Evaluate for parasitized red blood cells.
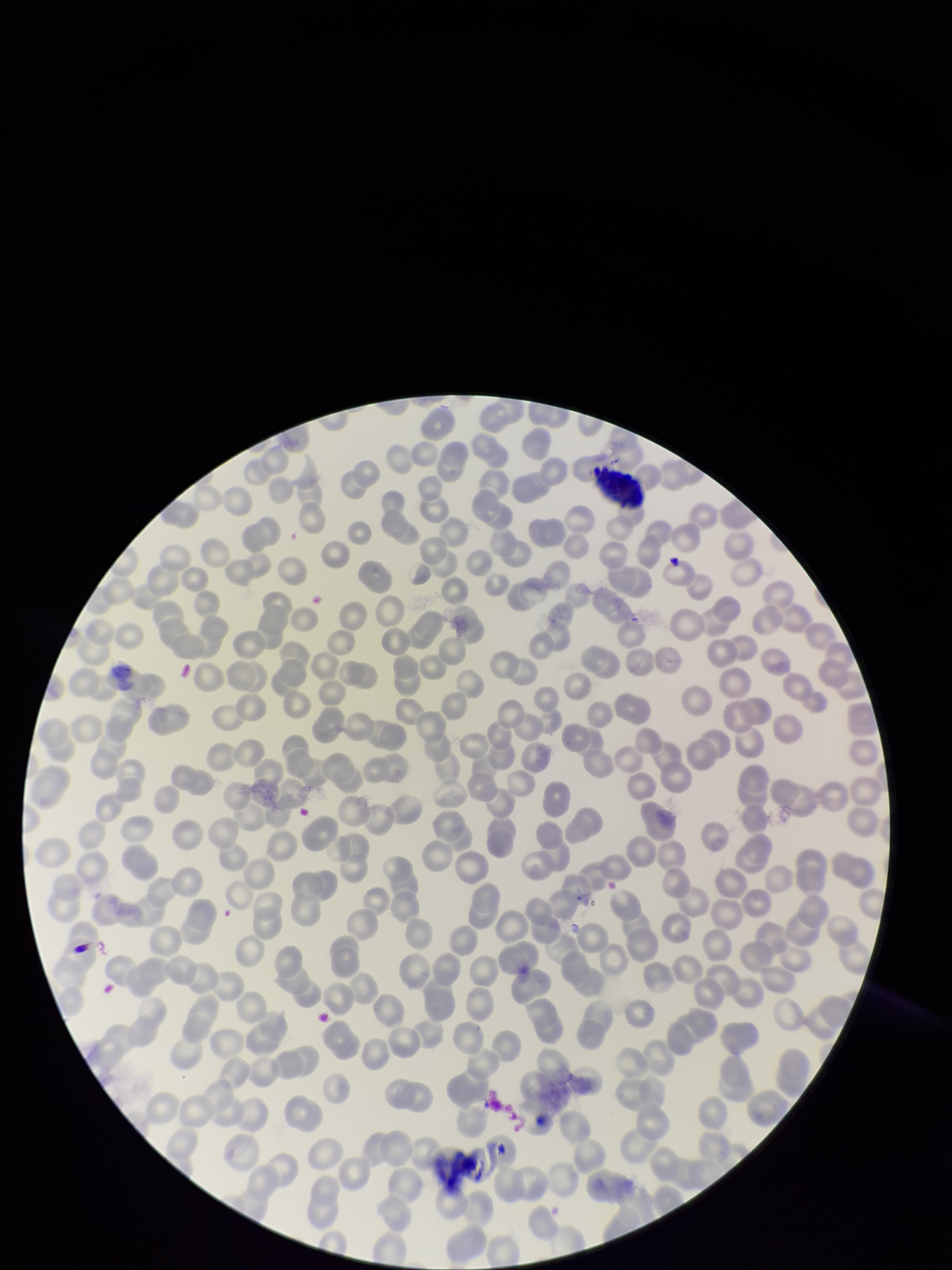
None detected.

Summary:
  - Stain: Giemsa
  - Preparation: thin smear
  - Image size: 952×1270 pixels
  - Patient malaria status: negative
  - Parasitized red blood cell count: 0
  - Capture: smartphone photograph through the microscope eyepiece
  - Field of view: one from this slide
  - Red blood cell count: 265